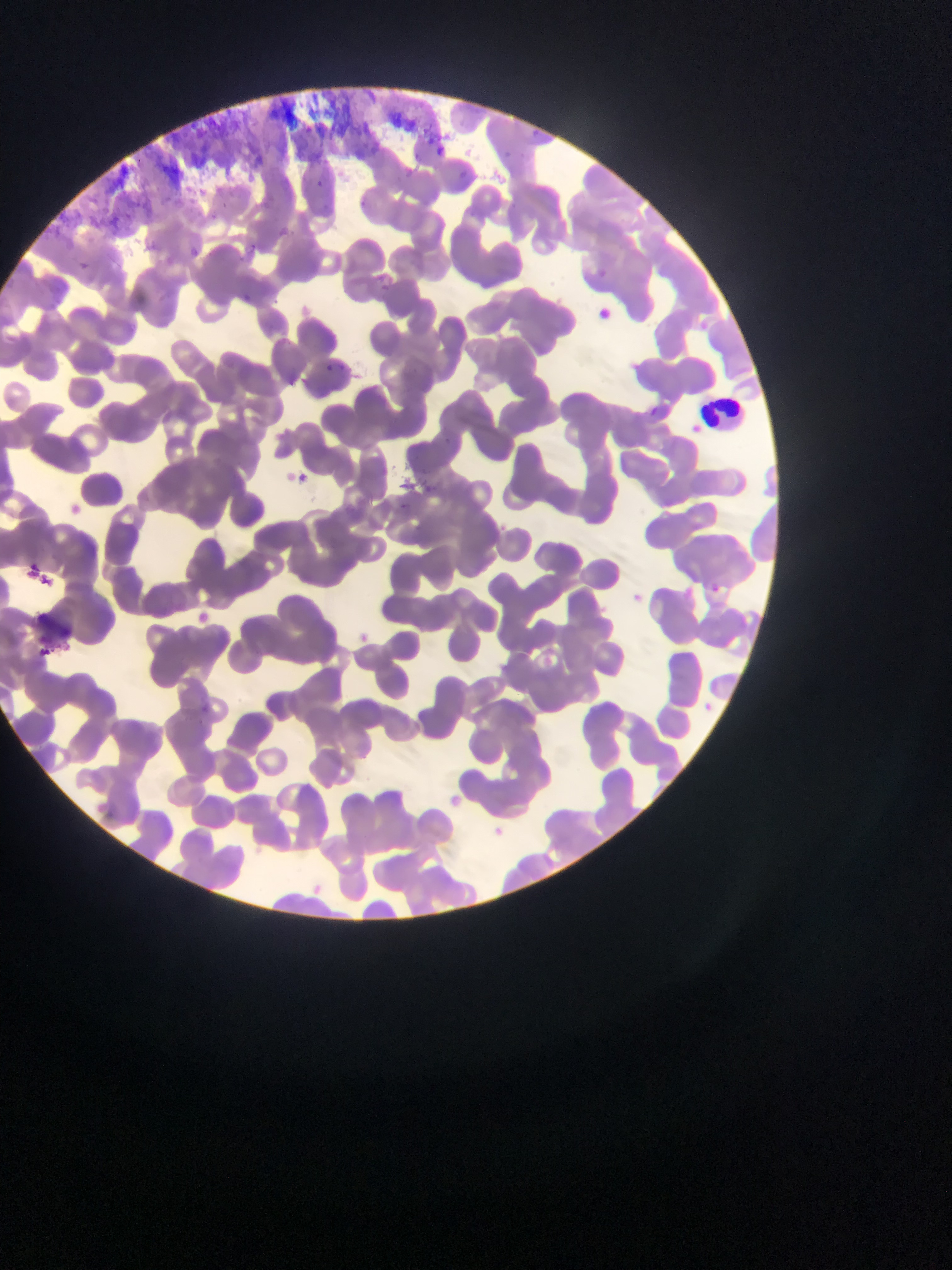
Approximate bounding boxes as (left, top, right, bottom) in pixels. Leukocyte locations: (702, 394, 747, 431). Thin blood film. Image is 952×1270 pixels. Single field of view. Collected in Ghana. Mobile-phone photograph taken through the microscope.